Comment on the morphology of the erythrocytes.
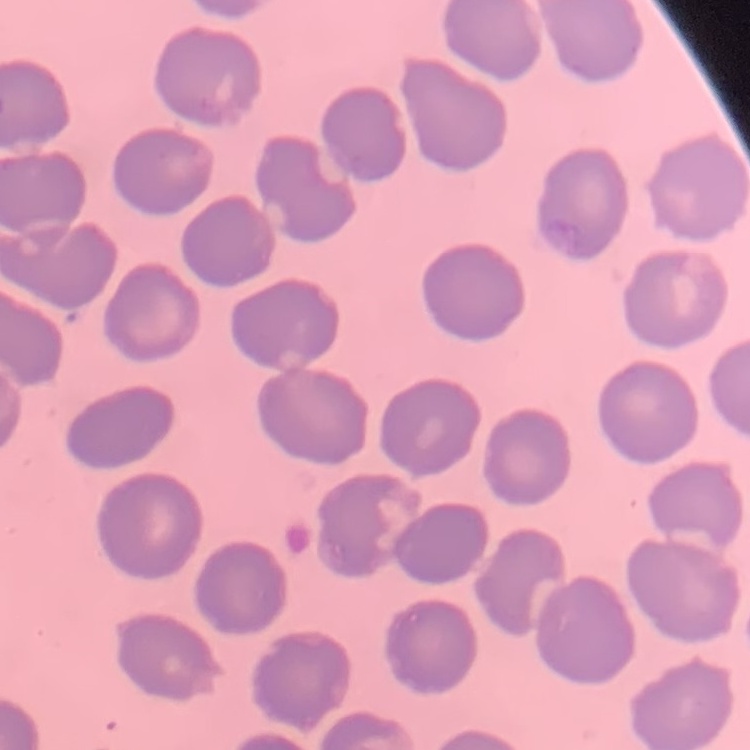

No rouleaux formation.

preparation = thin blood film
image type = one tile cut from a larger photomicrograph
stain = Field's or Giemsa